Comment on the morphology of the red blood cells.
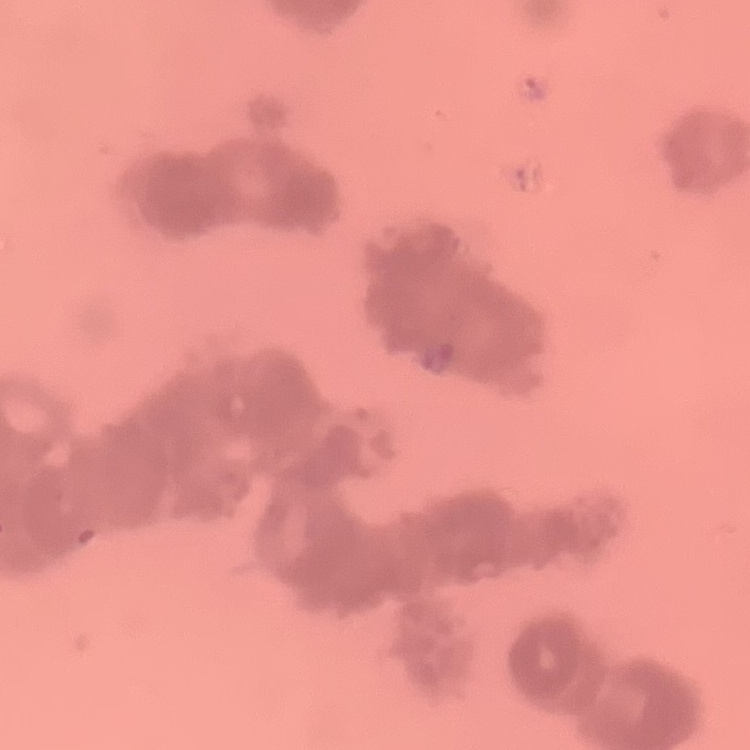
Rouleaux formation.

Thin blood smear. Stained with either Field's or Giemsa. One tile cut from a larger photomicrograph.